Point out each malaria parasite and each leukocyte.
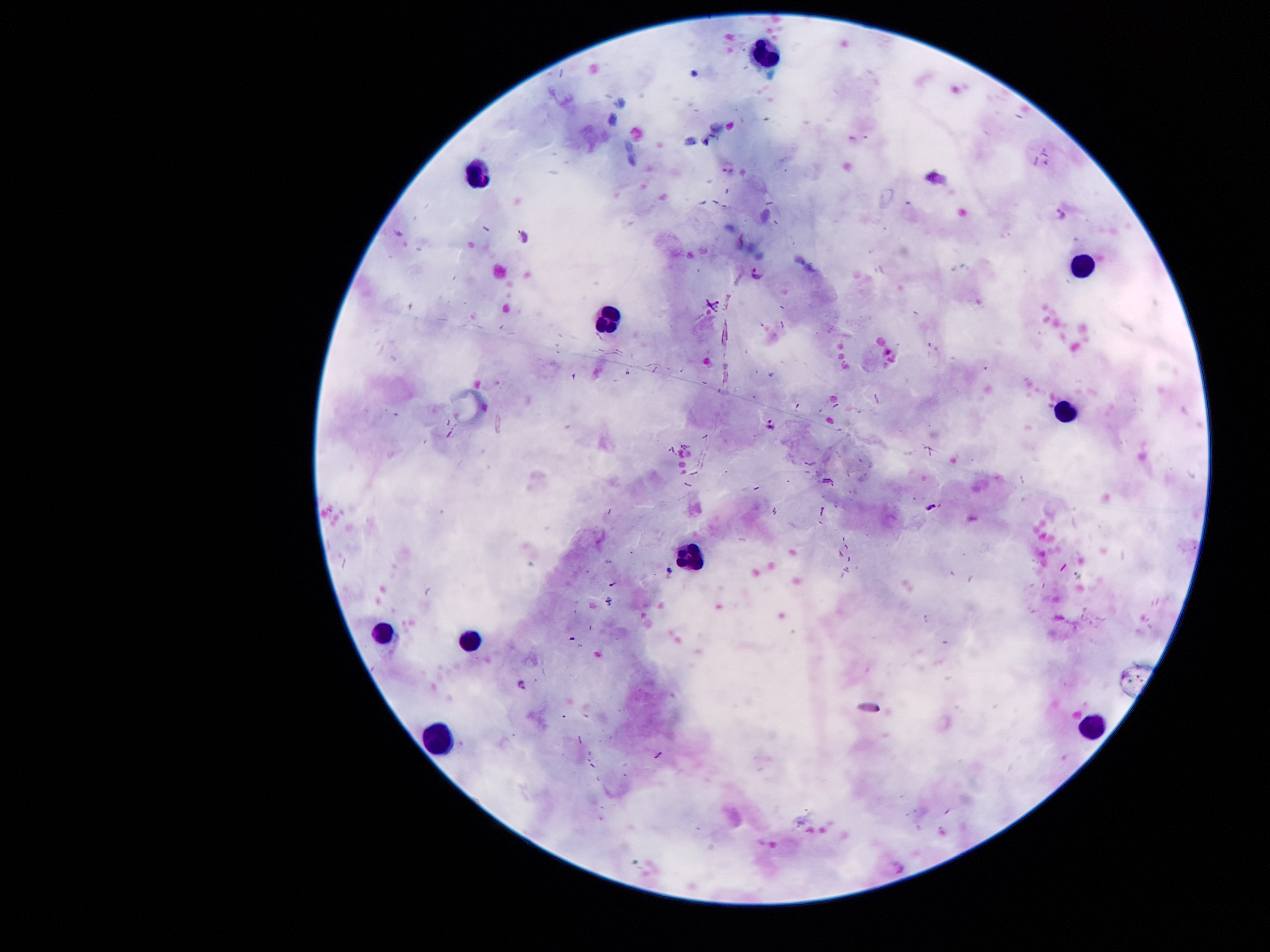

Approximate object centers, in pixels from the top-left corner.
Malaria parasites: (x=730, y=166), (x=1061, y=215), (x=526, y=236), (x=756, y=272), (x=770, y=422), (x=933, y=506).
Leukocytes: (x=764, y=57), (x=473, y=173), (x=1087, y=264), (x=605, y=323), (x=1067, y=413), (x=686, y=558), (x=379, y=633), (x=466, y=642), (x=1087, y=729), (x=437, y=742).

Patient malaria status: positive for Plasmodium falciparum. Thick blood smear. Smartphone photograph taken through the microscope eyepiece. Single field of view. Image is 1270×952 pixels. Giemsa-stained preparation. 100x magnification.